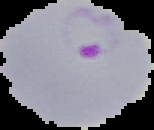

Summary:
  - Preparation: thin blood film
  - Malaria status: parasitized
  - Image type: segmented cell region with the area outside set to black
  - Image size: 154×130 pixels